Describe the morphology of the red blood cells.
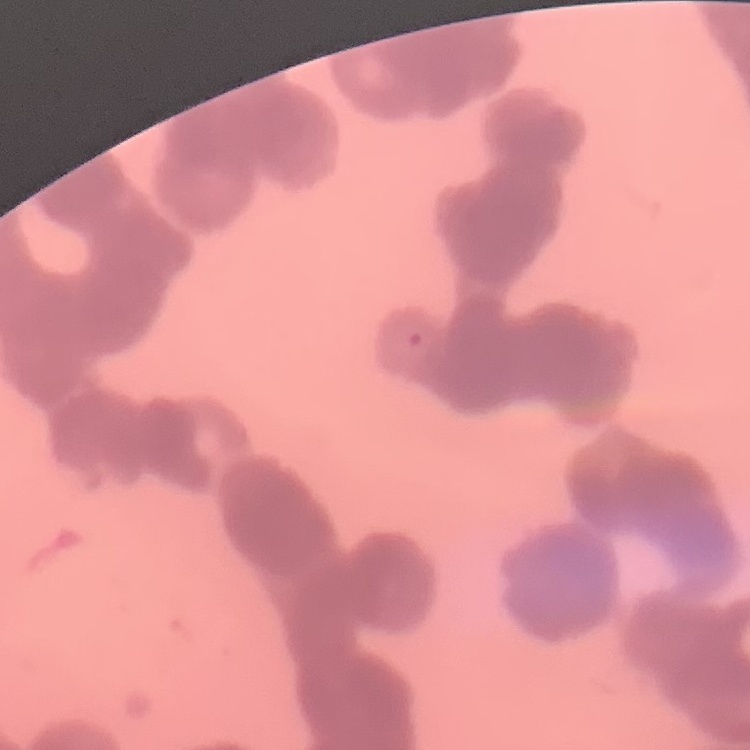
Rouleaux formation.

One tile cut from a larger photomicrograph. Stained with either Field's or Giemsa. Thin blood film.